Locate every Plasmodium parasite.
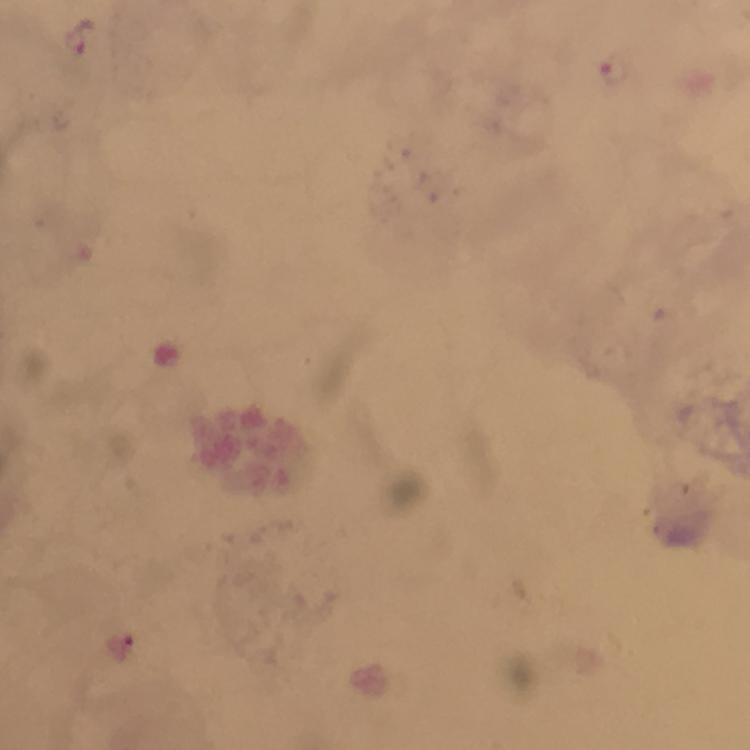
Approximate centers as [x, y] in pixels.
Plasmodium parasites: [83, 37], [616, 67].

cropped_from: one field of view
context: from a malaria diagnostic workup
preparation: thick blood film
magnification: 100x
capture: smartphone photograph through a microscope
image_size: 750×750 pixels
immersion_oil: used
stain: Giemsa